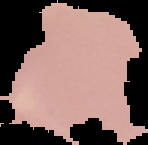
Image is 148×145 pixels. From a thin blood smear. Segmented cell region on a black background. Malaria status: uninfected.